Point out each leukocyte.
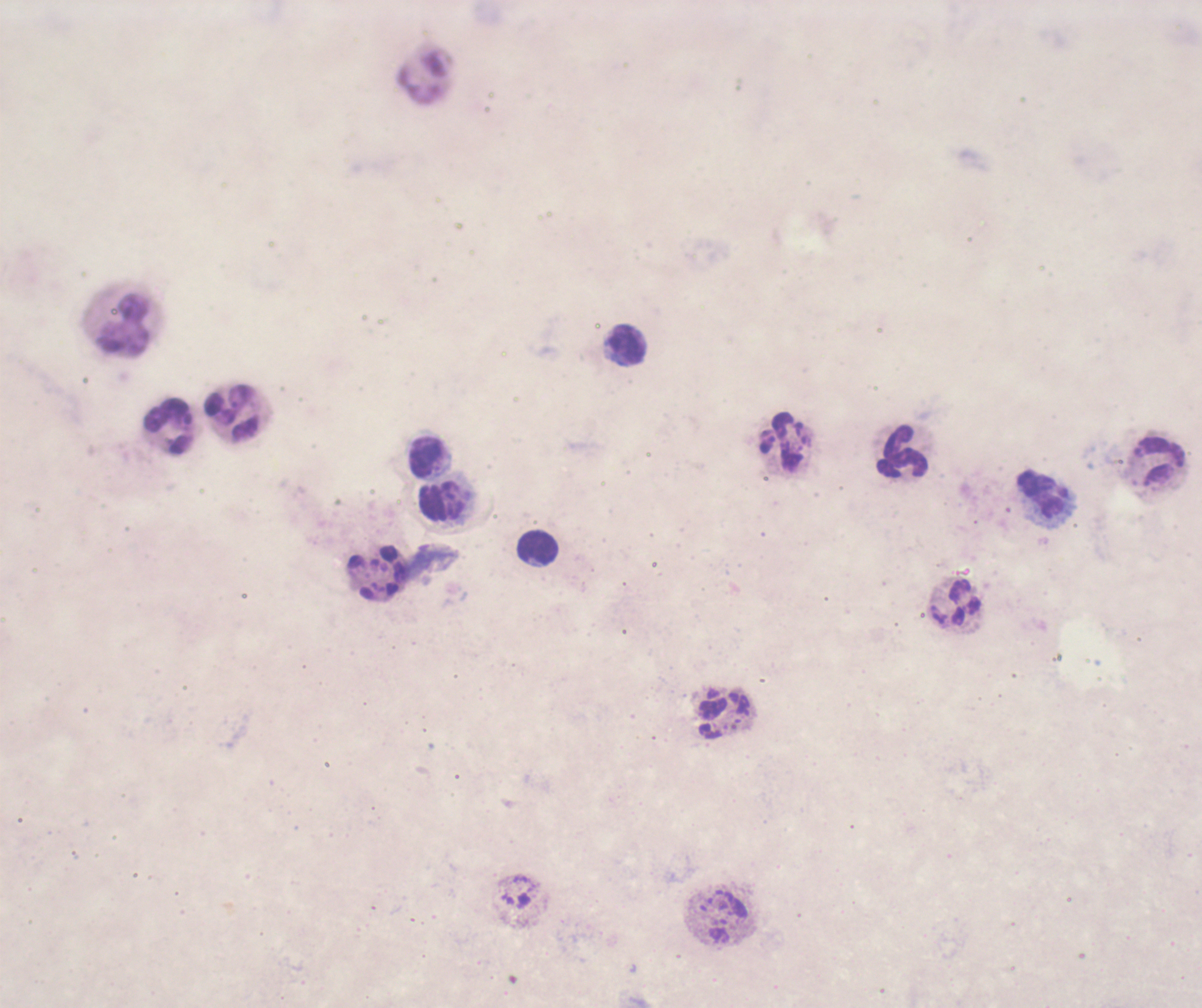

Approximate centers as (x, y) in pixels.
Leukocytes: (123, 324), (626, 346), (230, 414), (170, 425), (782, 443), (903, 452), (426, 456), (1162, 462), (1044, 495), (440, 502), (538, 548), (956, 603).

Result: negative for malaria parasites. Romanowsky stain. Captured at 100x magnification. Single field of view. Coloration quality: bad. Previously used in an actual diagnosis. Background quality: unsatisfactory. Thick blood smear. Image is 1202×1008 pixels.